Identify the parasite.
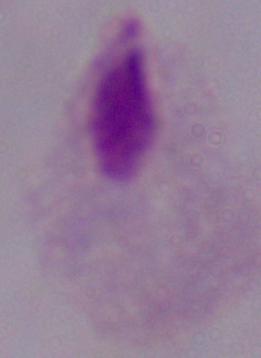

A trichomonad.

Micrograph. 1000x magnification.